Locate every Plasmodium parasite.
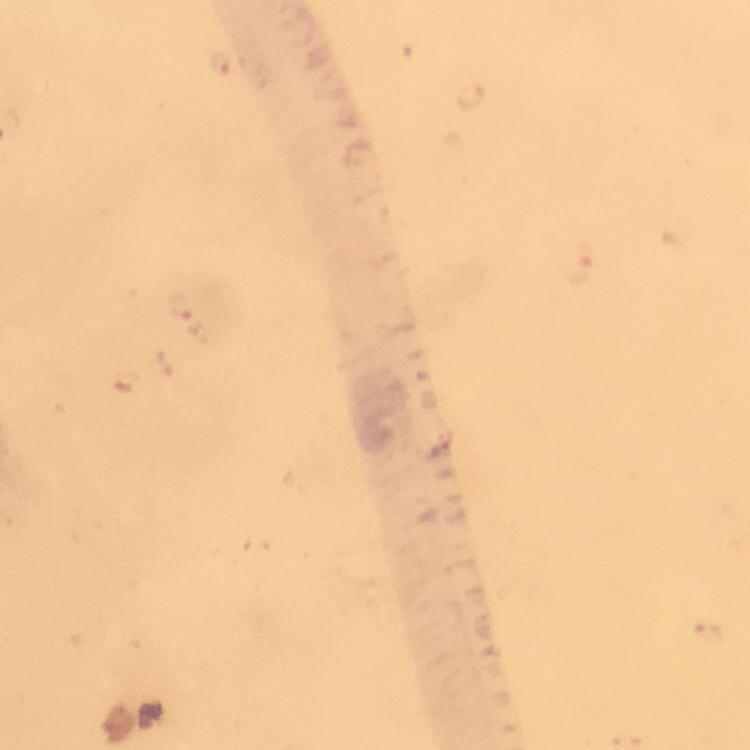
Approximate object centers, in pixels from the top-left corner.
Plasmodium parasites: (x=222, y=62), (x=472, y=96), (x=578, y=263), (x=184, y=308), (x=164, y=366), (x=125, y=383), (x=709, y=634).

Giemsa stain. From a diagnostic examination for malaria. A crop from one field of view. Photographed through the microscope with a smartphone camera. Thick smear. Immersion oil applied. Image is 750×750 pixels. 100x magnification.